Locate every Plasmodium parasite.
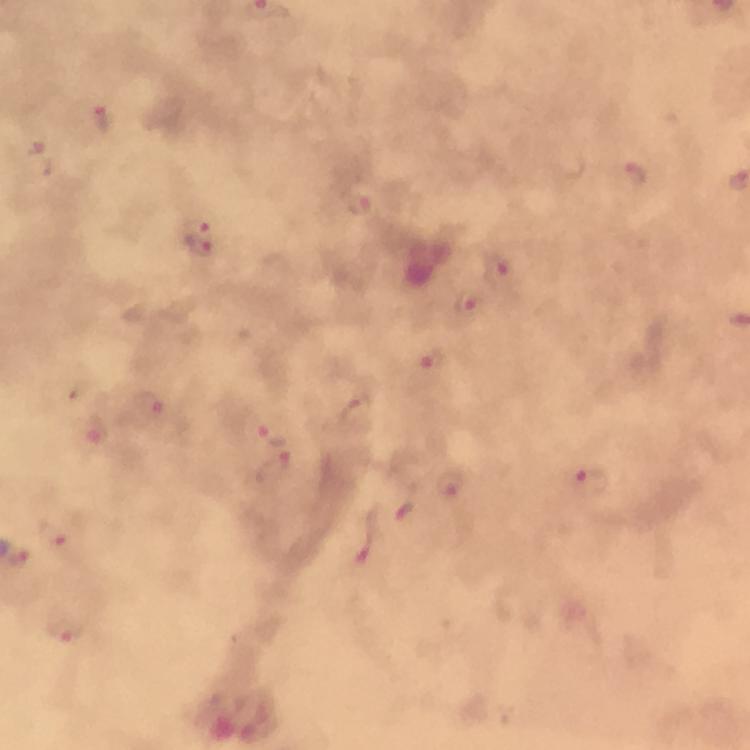
Approximate centers as {x, y} in pixels.
Plasmodium parasites: {102, 119}, {44, 163}, {634, 174}, {359, 206}, {201, 240}, {497, 267}, {469, 301}, {432, 362}, {150, 407}, {96, 430}, {271, 432}, {275, 468}, {591, 482}, {450, 490}, {406, 513}, {58, 539}, {365, 546}, {19, 561}, {64, 630}.

Photographed through the microscope with a smartphone camera. A crop from one field of view. Image is 750×750 pixels. Thick smear. At 100x magnification. From a malaria diagnostic workup. Giemsa-stained preparation. Immersion oil applied.